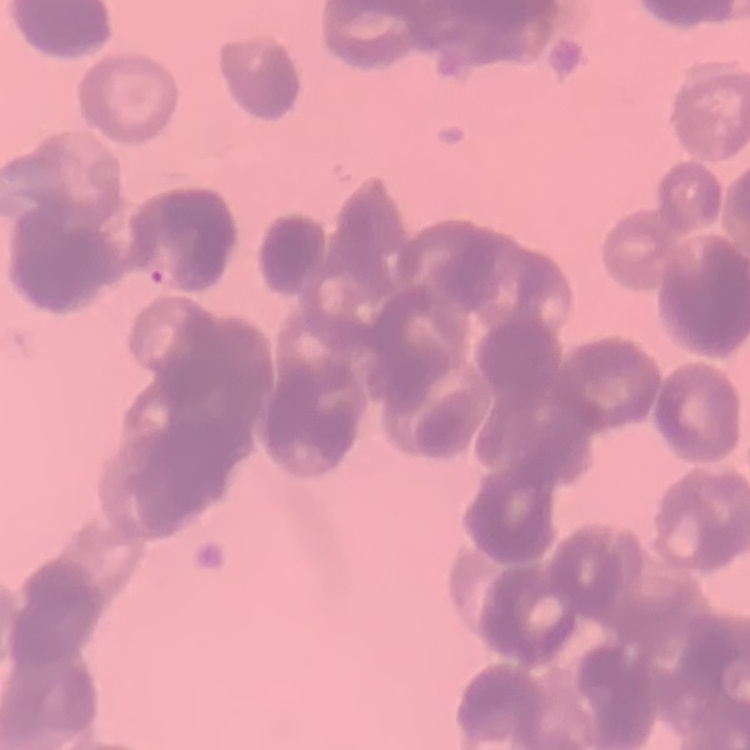
red blood cell morphology = rouleaux formation
stain = Field's or Giemsa
preparation = thin peripheral smear
image type = one tile cut from a larger photomicrograph